Describe the morphology of the erythrocytes.
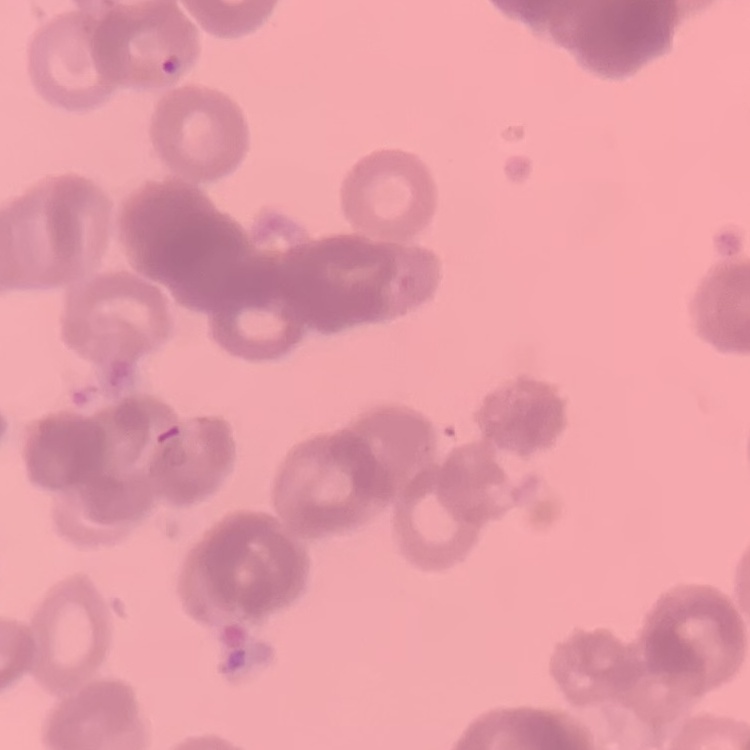
They show rouleaux formation.

Summary:
  - Image type: square crop of a larger photomicrograph
  - Stain: Field's or Giemsa
  - Preparation: thin blood smear